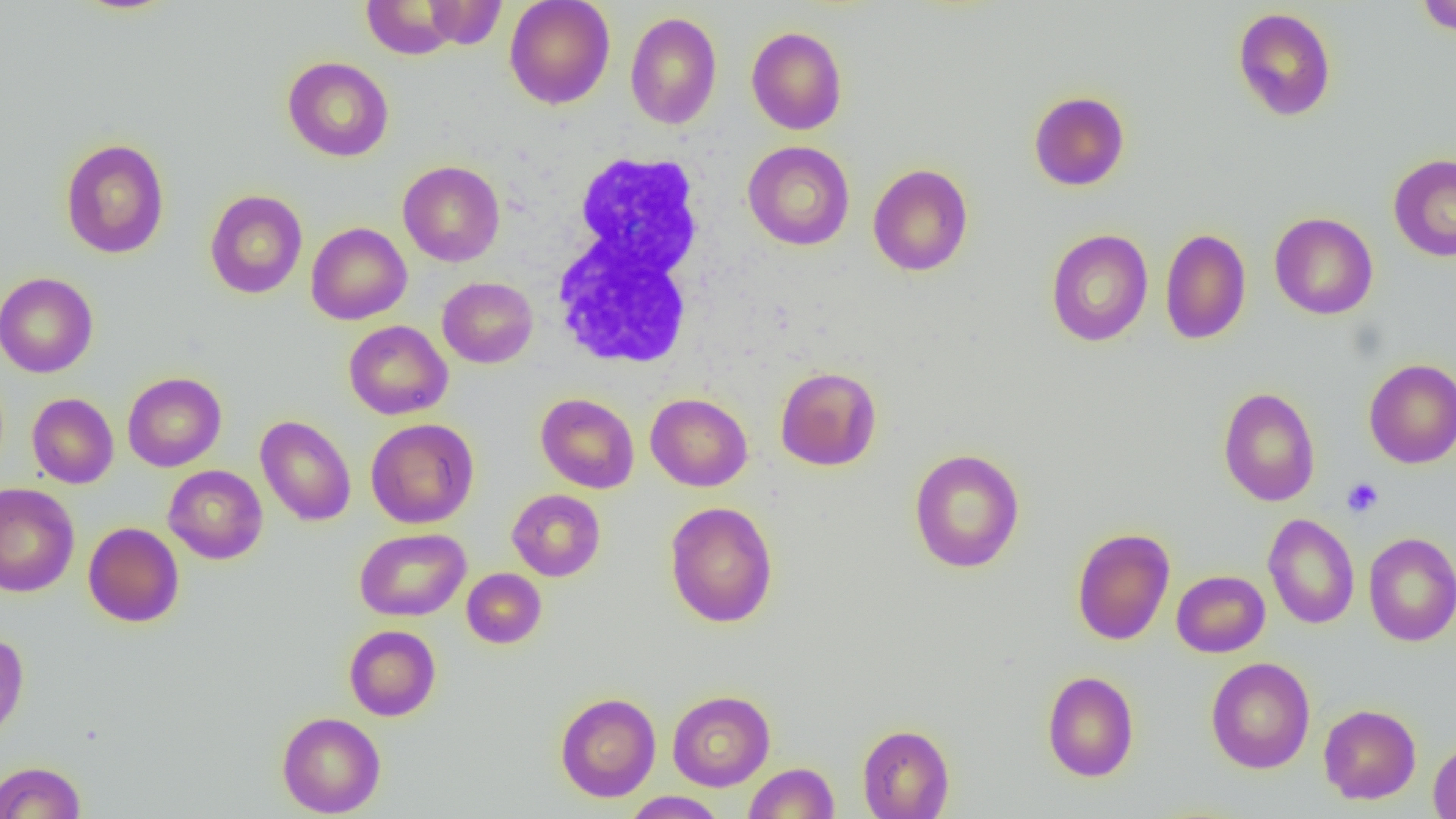

Summary:
  - Coordinate format: approximate bounding boxes as (x1, y1, x2, y2) in pixels
  - Uninfected red blood cell locations: (361, 0, 463, 59), (504, 0, 615, 109), (1414, 0, 1456, 36), (422, 1, 507, 49), (1232, 7, 1337, 121), (625, 11, 722, 130), (746, 26, 847, 135), (282, 56, 394, 162), (1028, 91, 1130, 191), (60, 138, 169, 259), (742, 141, 855, 250), (1388, 153, 1456, 262), (397, 160, 505, 266), (867, 163, 973, 276), (204, 190, 307, 298), (1269, 212, 1378, 319), (306, 222, 411, 325), (1159, 228, 1251, 345), (1045, 229, 1153, 347), (0, 272, 99, 377), (437, 276, 537, 368), (343, 320, 452, 420), (1364, 359, 1456, 468), (775, 366, 882, 471), (123, 372, 226, 471), (1218, 387, 1320, 506), (27, 393, 118, 488), (535, 393, 639, 493), (645, 393, 752, 491), (255, 415, 356, 526), (366, 418, 479, 529), (909, 447, 1025, 574), (164, 465, 267, 564), (0, 483, 79, 597), (507, 489, 605, 581), (664, 501, 778, 628), (1262, 513, 1359, 629), (83, 522, 184, 627), (1072, 526, 1175, 645), (355, 528, 471, 621), (1363, 532, 1456, 646), (461, 568, 547, 648), (1172, 570, 1270, 657), (344, 625, 441, 721), (0, 632, 29, 744), (1205, 656, 1315, 773), (1042, 670, 1139, 782), (667, 690, 775, 791), (555, 692, 661, 801), (1318, 703, 1421, 804), (277, 711, 386, 817), (857, 724, 955, 818), (1428, 738, 1456, 819), (0, 761, 86, 819), (744, 762, 839, 818), (622, 791, 727, 818)
  - White blood cell locations: (551, 150, 714, 373)
  - Platelet locations: (1342, 477, 1384, 518)
  - Slide-level diagnosis: no evidence of blood parasites
  - Field of view: one of a larger specimen
  - Preparation: thin blood film
  - Image size: 1456×819 pixels
  - Modality: light microscopy
  - Magnification: 1000x